Point out each malaria parasite.
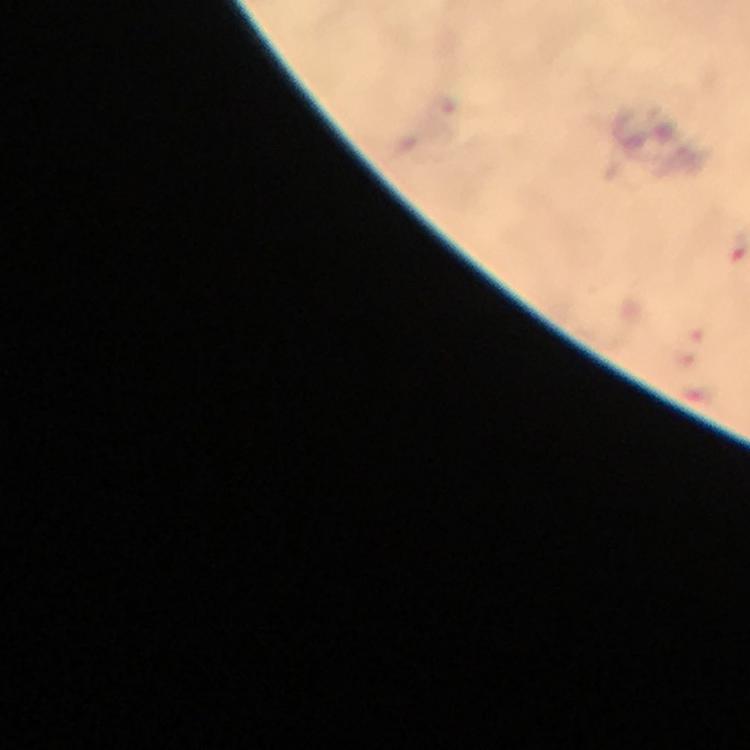
Approximate centers as (x, y) in pixels.
Malaria parasites: (697, 333), (684, 359).

A crop from one field of view. Giemsa-stained preparation. From a diagnostic examination for malaria. 100x magnification. Immersion oil was used. Thick blood film. Photographed through the microscope with a smartphone camera. Image is 750×750 pixels.